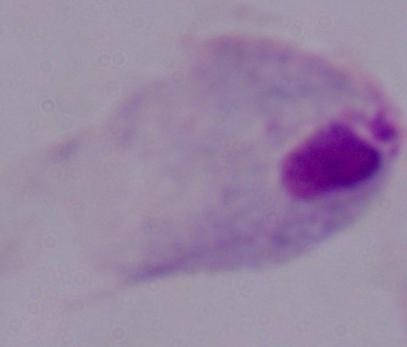
Summary:
  - Modality: micrograph
  - Magnification: 1000x
  - Identification: trichomonad